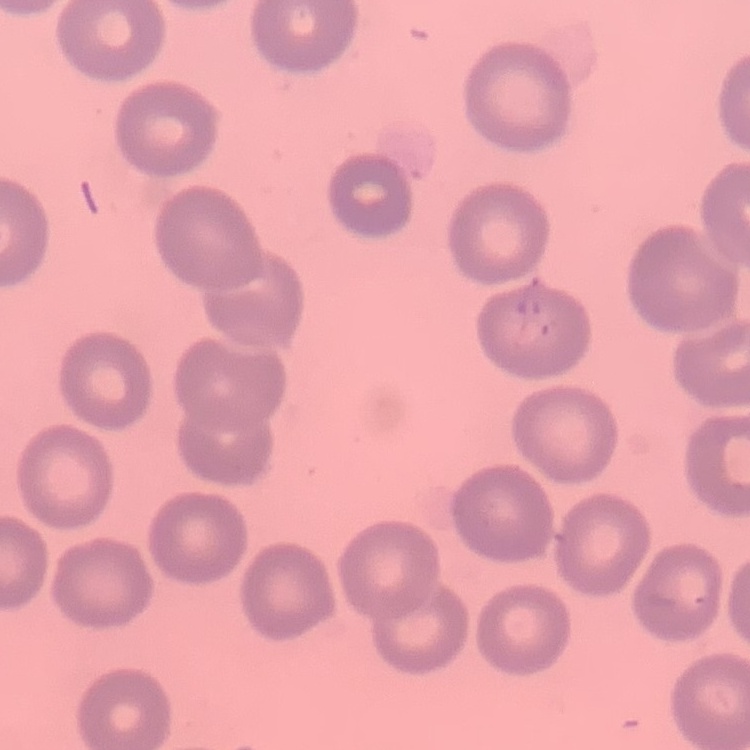
Summary:
  - Erythrocyte morphology: no rouleaux formation
  - Stain: Field's or Giemsa
  - Preparation: thin peripheral smear
  - Image type: square crop of a larger photomicrograph